Locate every blood parasite and identify its species.
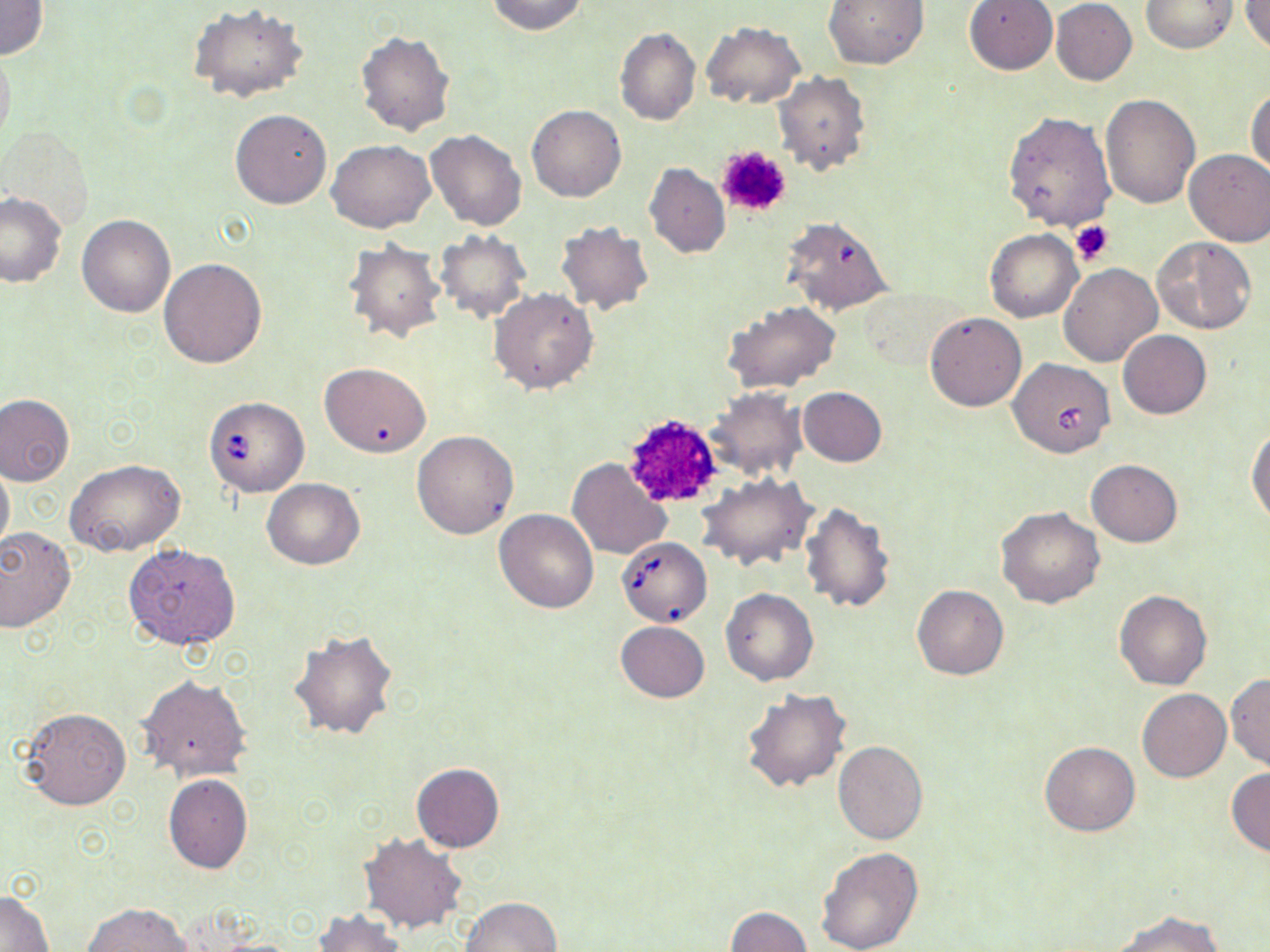
Approximate bounding boxes as (x1,y1)-(x2,y2) corner pairs in pixels.
Babesia divergens-infected red blood cells: (1008,358)-(1115,459), (203,396)-(309,497), (617,537)-(711,627).
No Plasmodium falciparum, Plasmodium ovale, Plasmodium malariae, Plasmodium vivax, or Trypanosoma brucei observed.

slide-level diagnosis = Babesia divergens
field of view = one of a larger specimen
uninfected red blood cell locations = approximate bounding boxes as (x1,y1)-(x2,y2) corner pairs in pixels: (0,0)-(48,60), (487,0)-(587,36), (823,0)-(929,70), (963,0)-(1058,75), (1241,0)-(1270,54), (1051,1)-(1137,85), (1141,1)-(1239,53), (188,4)-(308,104), (700,22)-(805,108), (614,27)-(700,126), (356,31)-(456,136), (0,41)-(15,151), (772,71)-(871,176), (1246,86)-(1269,179), (1100,93)-(1199,208), (527,105)-(626,202), (230,108)-(332,209), (1003,111)-(1115,231), (426,129)-(526,231), (327,140)-(434,233), (1184,148)-(1270,245), (644,163)-(730,259), (0,191)-(67,287), (76,214)-(174,318), (780,215)-(895,315), (556,222)-(654,315), (985,228)-(1082,322), (435,229)-(531,322), (1152,237)-(1258,334), (344,240)-(445,343), (160,258)-(267,368), (1058,263)-(1162,367), (489,288)-(598,394), (724,301)-(840,392), (925,312)-(1027,411), (1118,329)-(1211,419), (318,362)-(432,457), (706,386)-(808,482), (797,387)-(886,467), (0,394)-(74,486), (1247,427)-(1270,529), (411,430)-(519,539), (567,457)-(672,559), (65,458)-(185,557), (1,459)-(14,555), (1086,459)-(1182,547), (697,473)-(816,571), (261,478)-(365,569), (800,502)-(896,614), (998,506)-(1103,608), (494,509)-(598,613), (0,527)-(76,631), (123,544)-(240,650), (911,584)-(1009,680), (721,589)-(819,686), (1114,589)-(1212,689), (615,622)-(709,703), (289,629)-(399,742), (1226,673)-(1270,771), (137,674)-(252,781), (1137,687)-(1231,782), (742,688)-(851,794), (18,708)-(131,810), (833,741)-(928,846), (1039,741)-(1141,836), (410,762)-(505,852), (1226,768)-(1270,857), (163,774)-(253,874), (358,833)-(468,934), (816,846)-(924,952), (1,891)-(54,951), (461,897)-(561,952), (82,903)-(191,952), (725,906)-(810,952), (312,907)-(407,952), (1110,909)-(1224,952)
platelet locations = approximate bounding boxes as (x1,y1)-(x2,y2) corner pairs in pixels: (715,146)-(792,218), (1068,220)-(1113,266), (619,412)-(725,510)
stain = May-Grünwald-Giemsa
preparation = thin blood film
magnification = 1000x
modality = light microscopy
image size = 1270×952 pixels